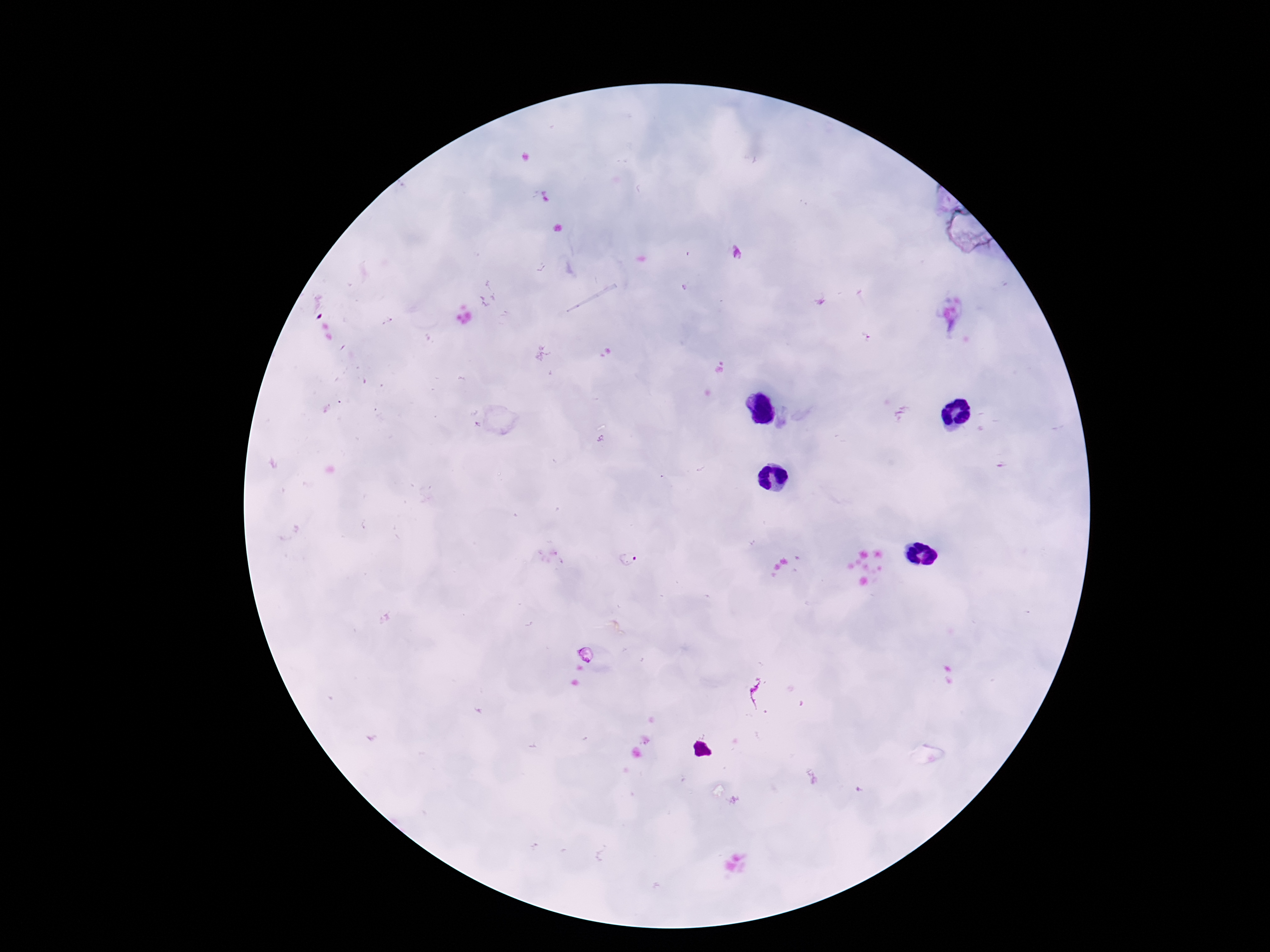
Approximate centers as [x, y] in pixels.
Summary:
  - Plasmodium parasite locations: [386, 321], [867, 338], [628, 559]
  - Stain: Giemsa
  - Magnification: 100x
  - Patient malaria status: positive
  - Image size: 1270×952 pixels
  - Capture: smartphone camera through the microscope eyepiece
  - Field of view: single
  - Preparation: thick blood smear